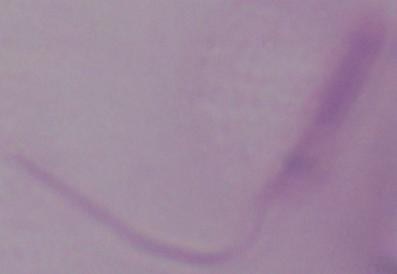
Summary:
  - Identification: Leishmania
  - Modality: micrograph
  - Magnification: 1000x